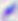
modality: photomicrograph
identification: Toxoplasma gondii
magnification: 400x